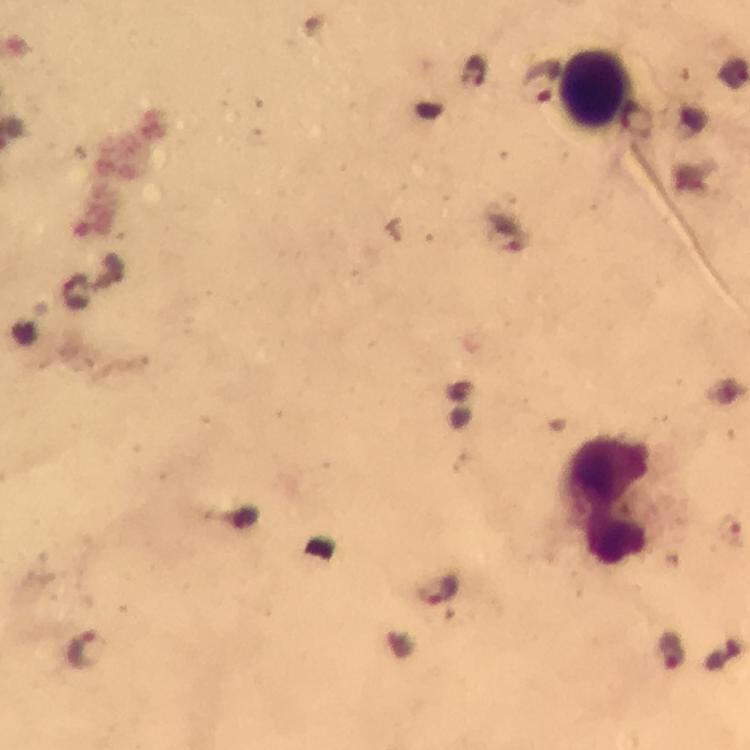
Approximate centers as {x, y} in pixels.
Summary:
  - Leukocyte locations: {595, 89}, {608, 502}
  - Plasmodium parasite locations: {472, 70}, {542, 82}, {439, 587}, {88, 649}, {671, 650}
  - Image size: 750×750 pixels
  - Capture: smartphone camera through the microscope
  - Cropped from: a single field of view
  - Preparation: thick smear
  - Context: from a diagnostic examination for malaria
  - Stain: Giemsa
  - Magnification: 100x
  - Immersion oil: used